Locate every blood parasite and identify its species.
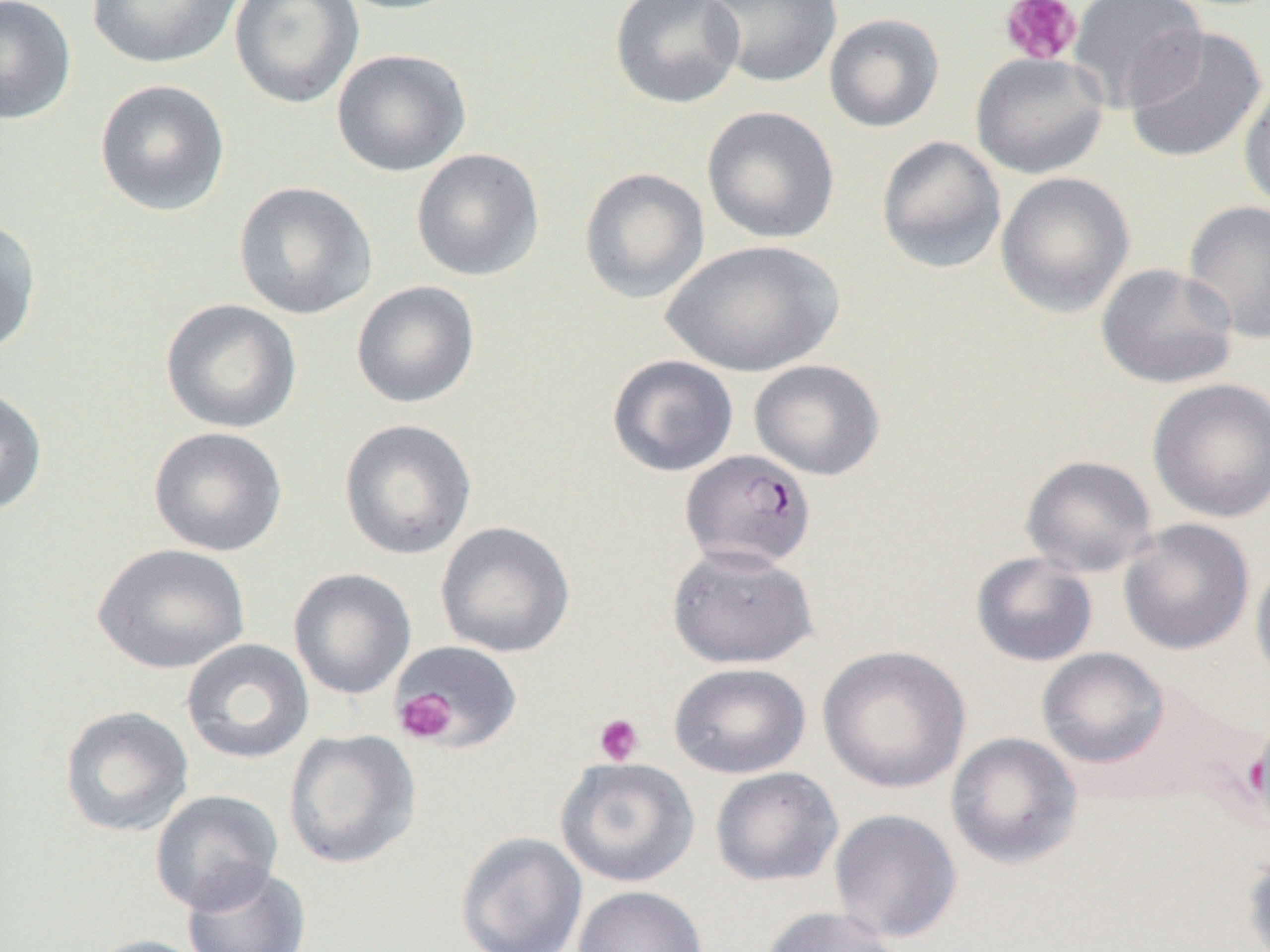
Approximate bounding boxes as (x1,y1)-(x2,y2) corner pairs in pixels.
Plasmodium falciparum-infected red blood cells: (680,449)-(816,570).
No Plasmodium ovale, Plasmodium malariae, Plasmodium vivax, Babesia divergens, or Trypanosoma brucei observed.

Summary:
  - Platelet locations: (1000,0)-(1083,66), (395,689)-(458,744), (594,713)-(645,766)
  - Uninfected red blood cell locations: (0,0)-(77,124), (85,0)-(244,69), (229,0)-(365,109), (330,0)-(473,16), (609,0)-(745,109), (704,0)-(843,89), (1068,0)-(1208,113), (823,13)-(945,132), (1124,26)-(1268,164), (331,48)-(471,177), (970,52)-(1109,179), (1238,77)-(1270,212), (94,79)-(230,217), (701,106)-(840,244), (876,136)-(1007,275), (411,148)-(545,282), (578,167)-(710,304), (995,171)-(1135,317), (232,181)-(378,320), (1182,199)-(1270,344), (0,217)-(42,355), (662,239)-(844,377), (1095,263)-(1239,389), (351,281)-(480,409), (159,298)-(302,434), (607,354)-(739,476), (748,359)-(885,480), (1147,378)-(1270,523), (0,387)-(48,515), (339,419)-(477,560), (148,426)-(287,557), (1020,454)-(1158,577), (1118,518)-(1255,655), (435,521)-(575,658), (93,543)-(250,674), (666,544)-(818,669), (970,552)-(1098,667), (1250,557)-(1270,689), (288,568)-(417,700), (181,638)-(315,764), (391,641)-(523,750), (817,644)-(972,793), (1036,648)-(1169,768), (669,662)-(811,778), (59,705)-(194,837), (284,728)-(421,869), (945,732)-(1083,869), (555,757)-(699,887), (710,766)-(843,887), (150,789)-(284,914), (828,808)-(963,944), (455,832)-(587,952), (1241,845)-(1270,952), (182,863)-(312,952), (572,885)-(707,952), (759,906)-(904,952), (80,934)-(214,952)
  - Slide-level diagnosis: Plasmodium falciparum
  - Modality: light microscopy
  - Magnification: 1000x
  - Field of view: one of a larger specimen
  - Preparation: thin blood smear
  - Image size: 1270×952 pixels